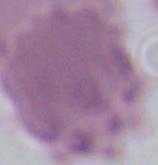
Summary:
  - Identification: erythrocyte
  - Magnification: 1000x
  - Modality: micrograph